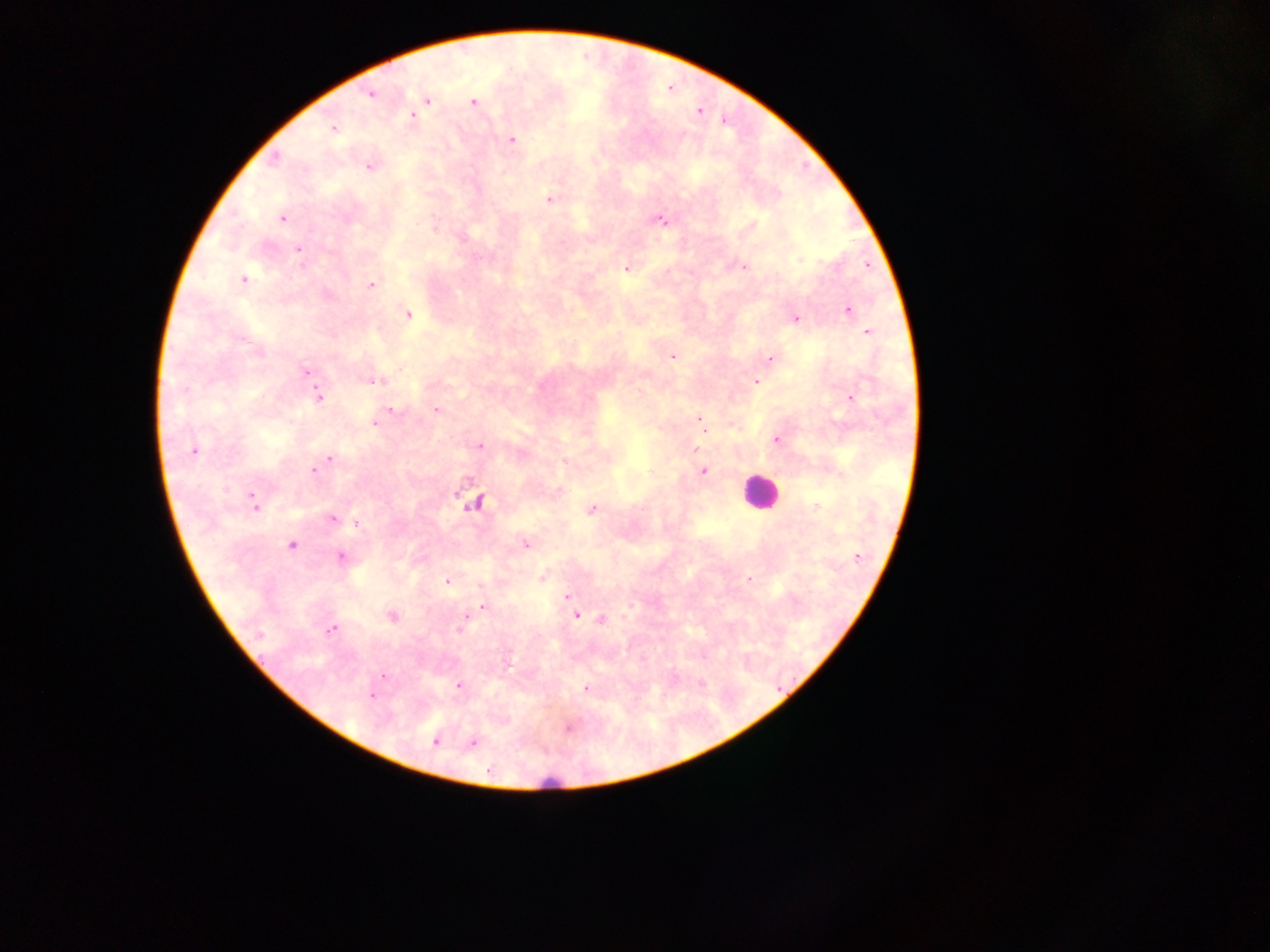
field of view = single
country = Ghana
leukocyte locations = approximate centers as [x, y] in pixels: [760, 493], [547, 782]
Plasmodium parasite locations = approximate centers as [x, y] in pixels: [370, 94], [427, 100], [474, 101], [412, 117], [333, 128], [511, 140], [370, 165], [549, 199], [281, 218], [661, 220], [297, 250], [800, 260], [742, 266], [627, 267], [243, 279], [371, 285], [847, 310], [406, 314], [794, 318], [867, 332], [672, 356], [770, 359], [305, 372], [374, 380], [756, 381], [318, 396], [851, 397], [436, 409], [387, 411], [377, 418], [700, 420], [703, 428], [776, 439], [479, 446], [193, 450], [329, 458], [319, 467], [314, 469], [703, 471], [253, 501], [475, 502], [591, 508], [333, 519], [357, 523], [291, 544], [526, 544], [340, 556], [543, 577], [749, 579], [447, 581], [567, 596], [483, 606], [575, 614], [465, 615], [392, 616], [602, 620], [331, 628], [460, 628], [383, 676], [459, 685], [587, 688], [371, 694], [569, 726], [434, 740], [472, 742]
preparation = thick blood smear
capture = mobile-phone photograph through a microscope
image size = 1270×952 pixels